Name the parasite shown.
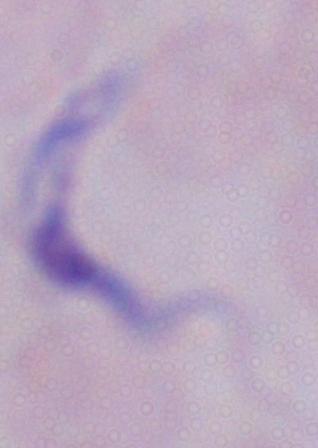

This is a trypanosome.

modality = photomicrograph
magnification = 1000x